Assess this cell for malaria.
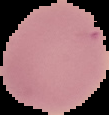
Uninfected.

{
  "image_size": "109×115 pixels",
  "preparation": "thin blood film",
  "image_type": "segmented cell region on a black background"
}